Assess the morphology of the red blood cells.
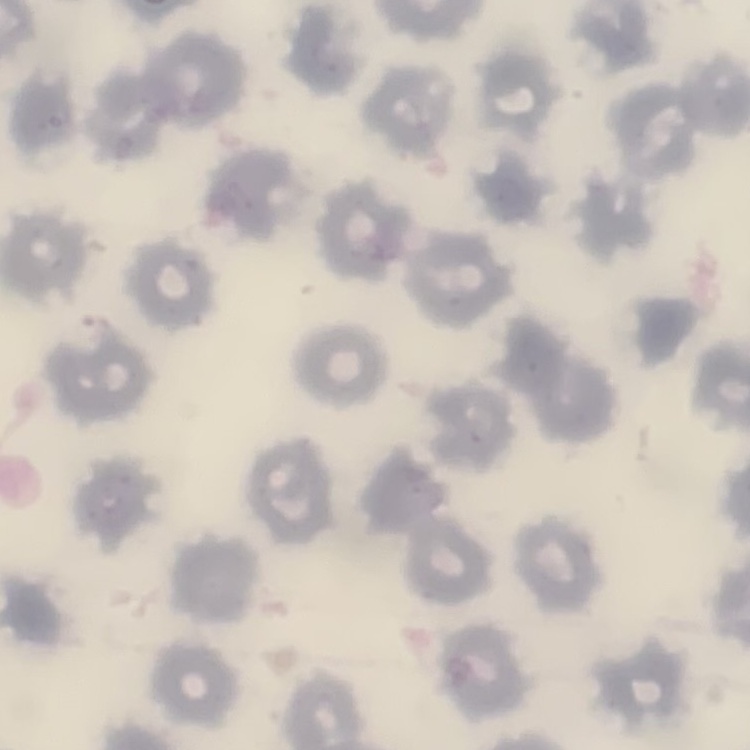
They show no rouleaux formation.

One tile cut from a larger photomicrograph. Thin peripheral smear. Field's or Giemsa stain.